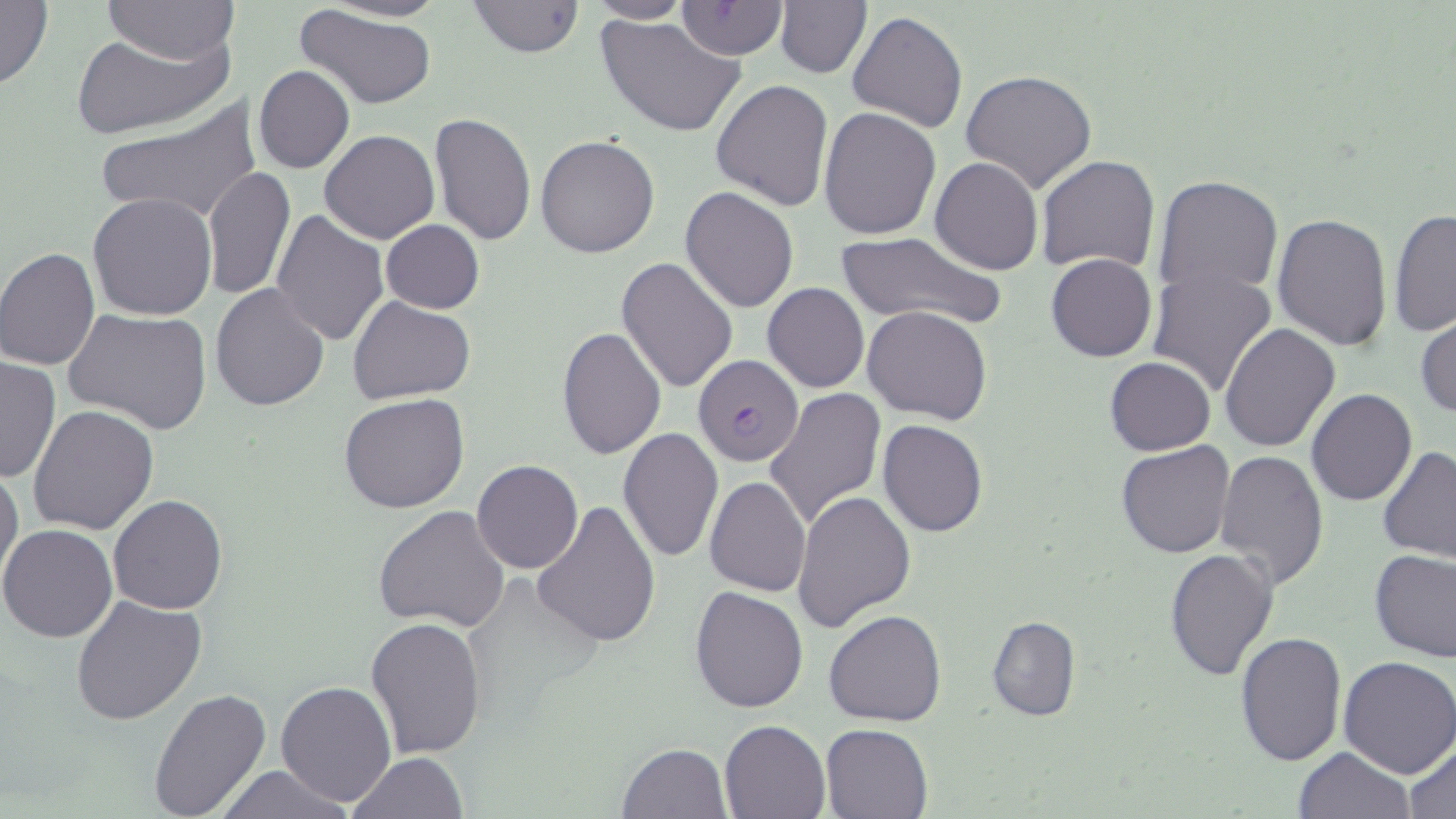
Summary:
  - Coordinate format: approximate bounding boxes as (x1,y1)-(x2,y2) corner pairs in pixels
  - Uninfected red blood cell locations: (0,0)-(53,91), (324,0)-(449,23), (465,0)-(585,57), (676,0)-(790,59), (105,1)-(236,65), (586,2)-(693,24), (775,2)-(871,77), (293,3)-(437,111), (847,10)-(966,132), (597,15)-(746,137), (72,27)-(233,140), (253,64)-(355,173), (959,67)-(1097,195), (711,79)-(835,213), (95,99)-(260,226), (819,108)-(941,240), (430,112)-(536,246), (318,130)-(440,243), (535,134)-(661,259), (1036,155)-(1160,274), (930,156)-(1044,274), (203,168)-(294,301), (1152,174)-(1283,303), (679,187)-(799,313), (87,192)-(219,321), (1389,208)-(1455,340), (271,210)-(389,346), (1272,213)-(1393,352), (380,220)-(485,314), (835,231)-(1005,329), (0,247)-(101,369), (1045,252)-(1158,362), (617,256)-(739,395), (1146,265)-(1278,399), (762,282)-(869,393), (211,283)-(329,411), (348,296)-(475,403), (63,305)-(212,435), (864,306)-(991,425), (1415,314)-(1456,418), (1219,323)-(1340,452), (556,328)-(667,461), (1,355)-(60,484), (1104,356)-(1216,455), (765,387)-(885,530), (1305,389)-(1417,507), (338,392)-(471,514), (28,403)-(160,536), (878,419)-(987,536), (617,427)-(723,563), (1115,439)-(1236,558), (1378,446)-(1456,563), (1214,449)-(1330,591), (0,461)-(23,591), (471,461)-(584,573), (705,475)-(811,595), (792,490)-(916,634), (108,494)-(228,614), (531,499)-(659,648), (374,504)-(511,633), (0,524)-(119,642), (1164,549)-(1280,683), (1369,549)-(1456,662), (689,586)-(809,714), (71,593)-(206,726), (824,609)-(947,728), (985,615)-(1080,723), (364,618)-(488,757), (1234,632)-(1347,766), (1337,655)-(1456,777), (276,680)-(396,806), (148,685)-(274,818), (719,718)-(832,819), (821,723)-(933,818), (1404,740)-(1456,818), (616,742)-(732,819), (1292,746)-(1417,819), (348,752)-(471,819), (209,765)-(358,819)
  - Plasmodium falciparum-infected red blood cell locations: (693,353)-(803,467)
  - Slide-level diagnosis: Plasmodium falciparum
  - Stain: May-Grünwald-Giemsa
  - Modality: optical microscopy
  - Image size: 1456×819 pixels
  - Field of view: single
  - Magnification: 1000x
  - Preparation: thin blood film